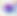
Summary:
  - Identification: Toxoplasma gondii
  - Modality: micrograph
  - Magnification: 400x